Assess the morphology of the red blood cells.
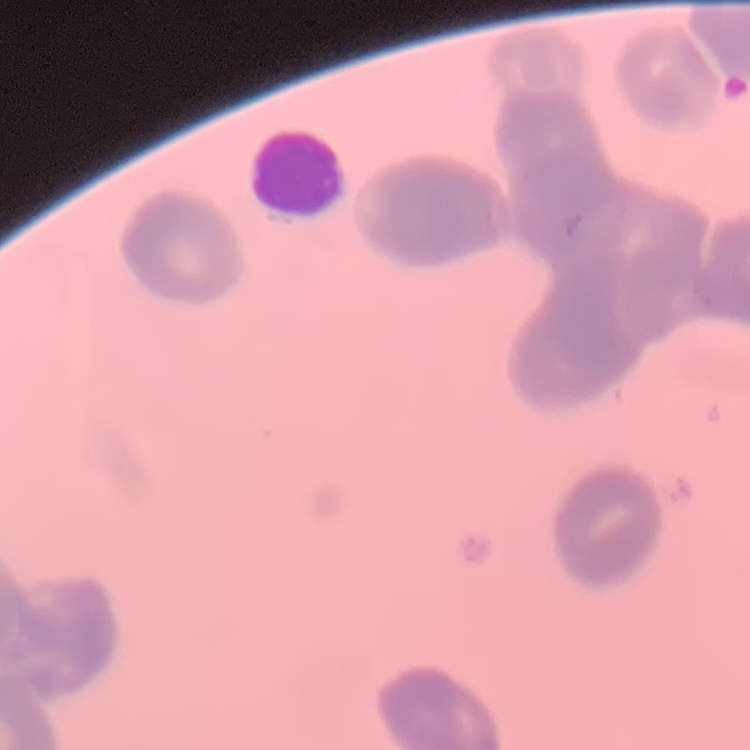
Rouleaux formation.

preparation = thin blood smear
stain = Field's or Giemsa
image type = one tile cut from a larger photomicrograph